Point out each malaria parasite.
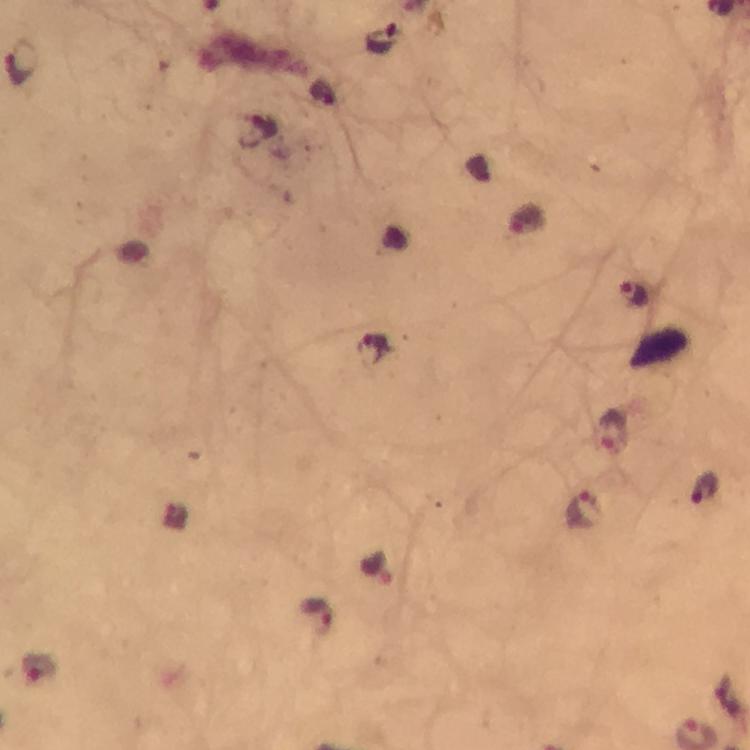

Approximate centers as [x, y] in pixels.
Malaria parasites: [382, 39], [22, 62], [261, 129], [633, 294], [614, 432], [705, 492], [582, 510], [378, 569], [316, 613].

Image is 750×750 pixels. 100x magnification. Immersion oil was used. Smartphone photograph taken through a microscope. From a diagnostic examination for malaria. Giemsa stain. Cropped region of a single field of view. Thick blood film.